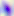

magnification = 400x
modality = photomicrograph
identification = Toxoplasma gondii